Describe the morphology of the erythrocytes.
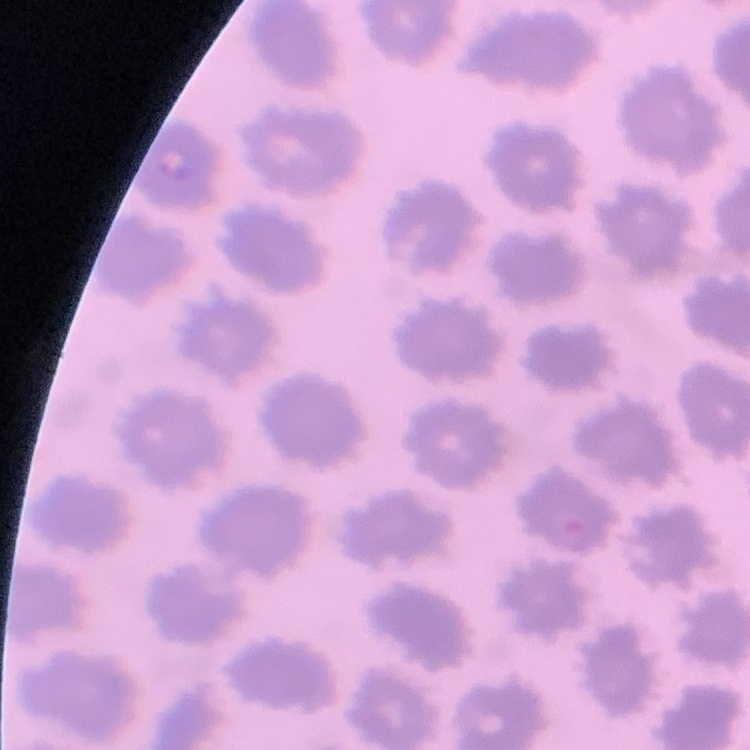
They show no rouleaux formation.

Summary:
  - Image type: one tile cut from a larger photomicrograph
  - Preparation: thin blood film
  - Stain: Field's or Giemsa